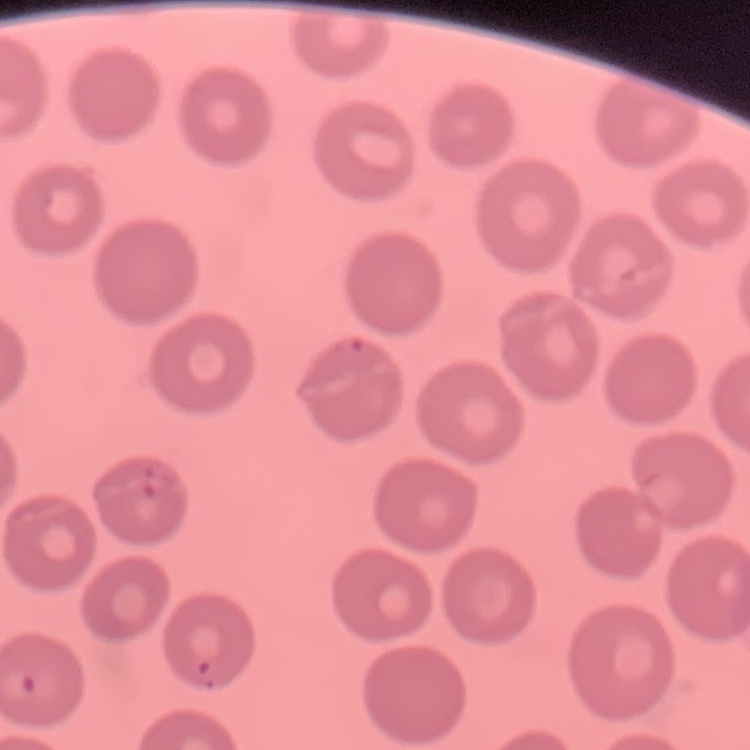

The erythrocytes exhibit no rouleaux formation. Thin blood smear. Square crop of a larger photomicrograph. Stained with either Field's or Giemsa.